Name the parasite shown.
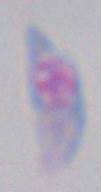

Toxoplasma gondii.

Micrograph. 1000x magnification.